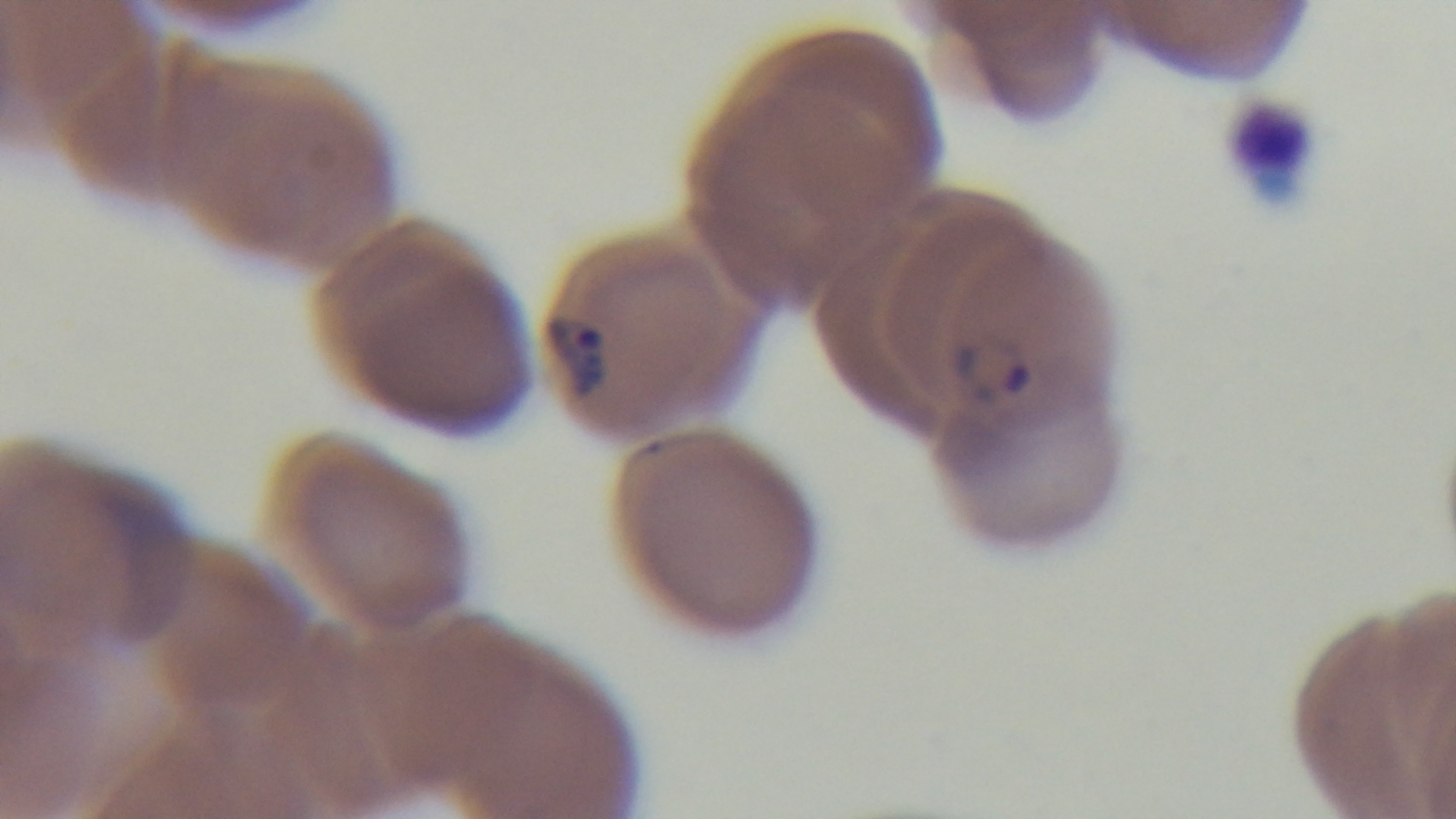

Summary:
  - Malaria status: infected
  - Objective: 100x oil immersion
  - Preparation: thin
  - Stain: Giemsa
  - Capture: mounted 4K digital camera
  - Modality: light microscopy
  - Field of view: single